Assess the morphology of the erythrocytes.
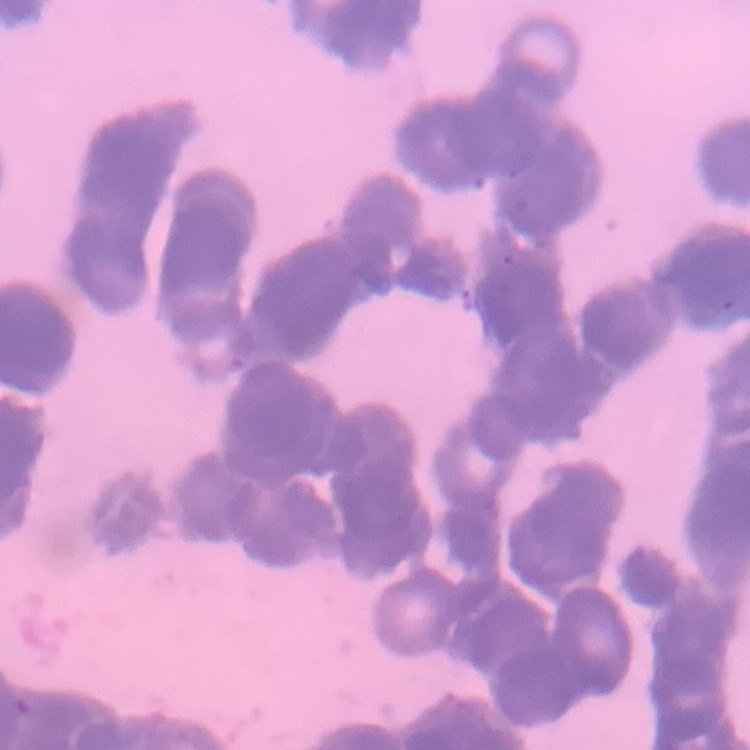

They show rouleaux formation.

preparation: thin blood smear
stain: Field's or Giemsa
image_type: square crop of a larger photomicrograph